Comment on the morphology of the red blood cells.
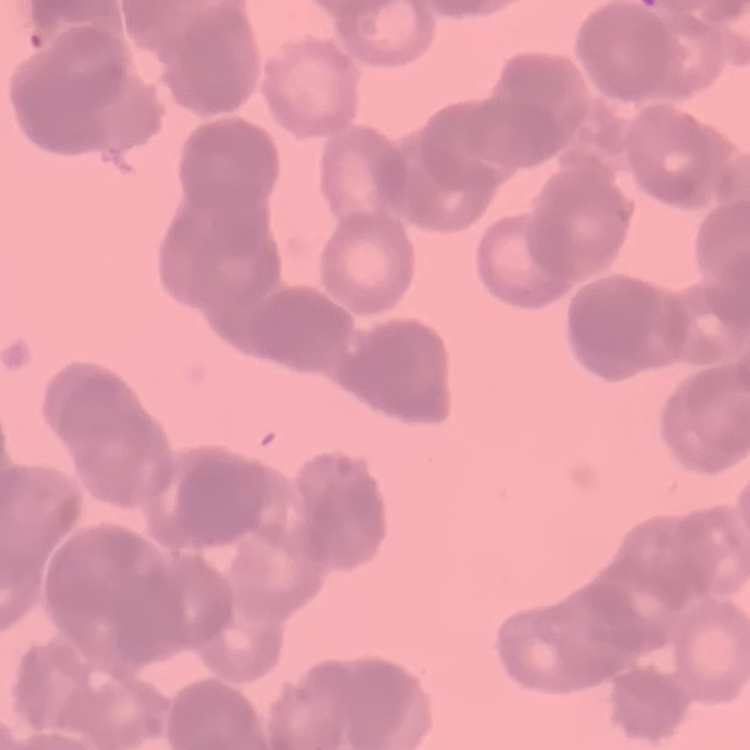

Rouleaux formation.

image type = one tile cut from a larger photomicrograph
stain = Field's or Giemsa
preparation = thin blood smear